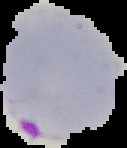
result = malaria parasites identified
image size = 127×148 pixels
preparation = thin blood smear
image type = cell region segmented out of the field of view; surrounding area masked to black